Outline each uninfected red blood cell.
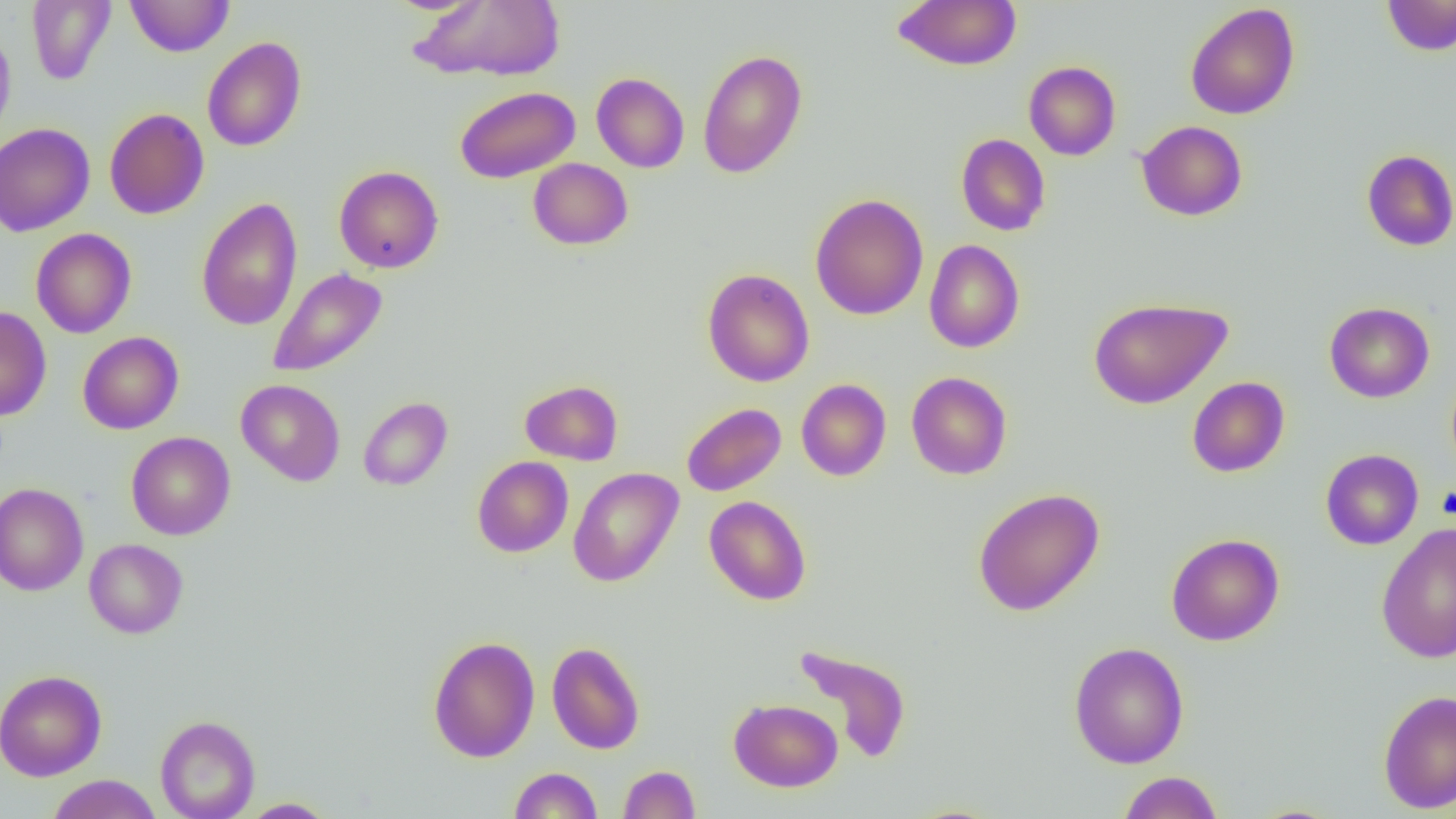

Approximate bounding boxes as (x1, y1, x2, y2) in pixels.
Uninfected red blood cells: (26, 0, 116, 85), (125, 0, 234, 57), (410, 0, 566, 82), (893, 0, 1022, 71), (1383, 0, 1456, 56), (1185, 3, 1300, 120), (0, 24, 16, 145), (202, 36, 307, 152), (697, 49, 808, 178), (1024, 61, 1121, 161), (591, 72, 689, 173), (454, 86, 580, 183), (104, 108, 209, 219), (1136, 120, 1248, 221), (0, 123, 95, 236), (955, 133, 1051, 236), (1361, 149, 1456, 251), (528, 158, 633, 250), (334, 165, 444, 273), (810, 194, 928, 320), (196, 197, 303, 331), (31, 228, 137, 338), (924, 239, 1024, 352), (267, 267, 388, 378), (702, 268, 814, 387), (1088, 297, 1232, 409), (1324, 302, 1435, 403), (0, 306, 52, 421), (78, 331, 184, 434), (906, 371, 1012, 479), (1187, 377, 1289, 477), (235, 379, 345, 486), (796, 379, 891, 481), (520, 380, 623, 465), (358, 397, 453, 490), (681, 402, 786, 496), (126, 432, 236, 540), (1321, 449, 1423, 550), (472, 456, 573, 558), (568, 467, 683, 588), (0, 482, 89, 596), (972, 487, 1105, 616), (704, 495, 812, 606), (1376, 522, 1456, 664), (1166, 533, 1284, 646), (84, 538, 188, 638), (427, 635, 540, 763), (547, 641, 645, 755), (1068, 641, 1189, 768), (793, 644, 912, 764), (0, 670, 107, 781), (1377, 689, 1455, 814), (729, 698, 842, 792), (155, 714, 260, 819), (619, 765, 700, 819), (508, 767, 602, 819), (1118, 771, 1224, 818), (46, 774, 162, 819), (238, 798, 338, 818).

Slide-level diagnosis: no evidence of blood parasites. Thin blood film. Image is 1456×819 pixels. Single field of view. Optical microscopy. Captured at 1000x magnification.